Report the malaria status of this cell.
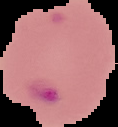

Parasitized.

{
  "image_type": "segmented cell region on a black background",
  "image_size": "118×127 pixels",
  "preparation": "thin blood smear"
}